Identify the blood parasite species.
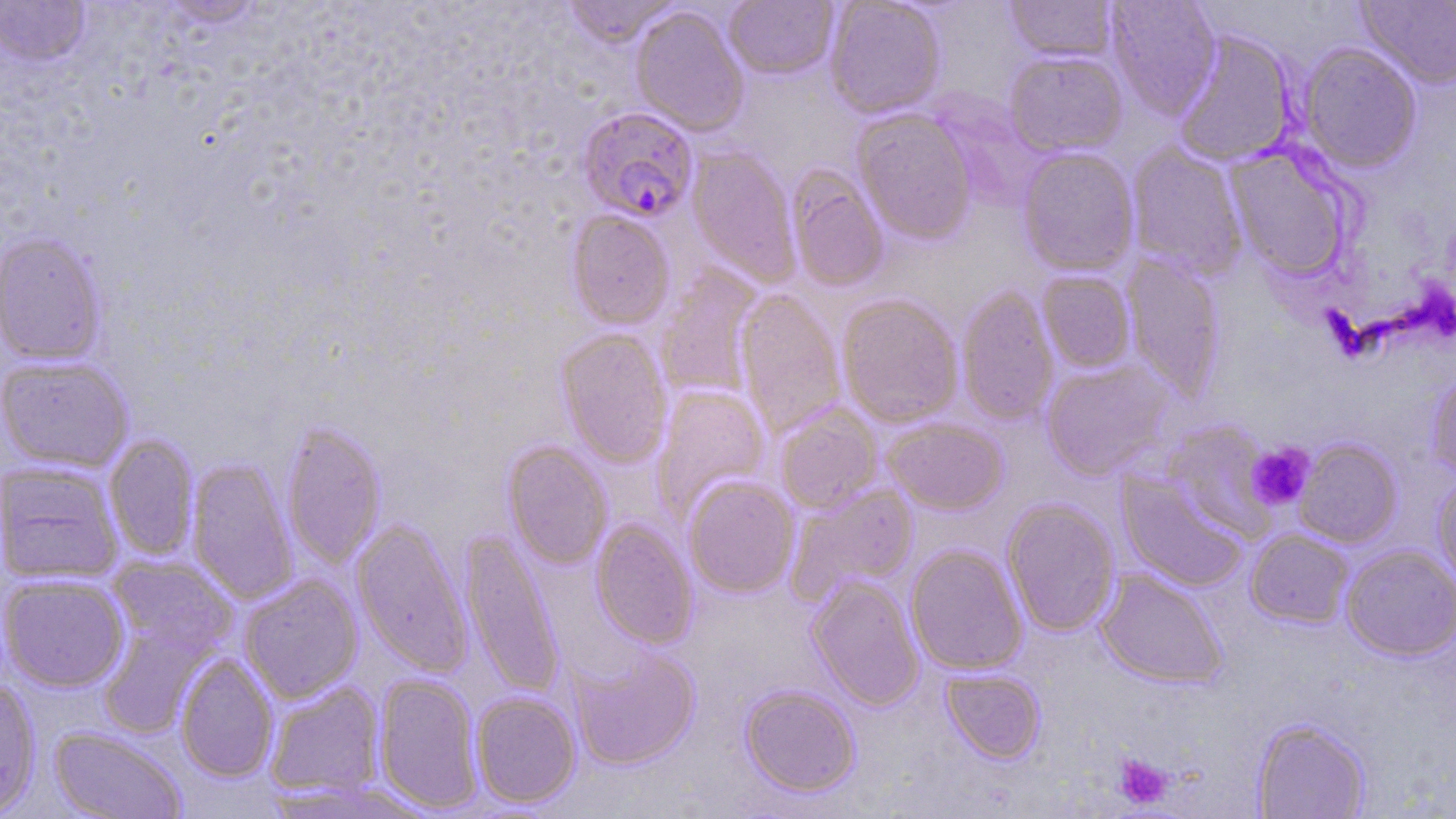
Plasmodium falciparum.

Summary:
  - Coordinate format: approximate bounding boxes as (x1,y1)-(x2,y2) corner pairs in pixels
  - Uninfected red blood cell locations: (561,0)-(681,49), (825,0)-(946,120), (1005,0)-(1117,63), (1105,0)-(1221,119), (1356,0)-(1456,89), (0,1)-(91,68), (154,1)-(268,29), (724,1)-(838,81), (630,6)-(749,137), (1172,29)-(1297,166), (1298,42)-(1422,172), (1003,51)-(1127,157), (853,108)-(978,245), (1127,144)-(1247,279), (1225,144)-(1356,282), (686,146)-(801,288), (1017,147)-(1140,277), (787,167)-(888,292), (566,211)-(675,330), (0,233)-(107,366), (1122,252)-(1225,401), (656,266)-(763,401), (1038,270)-(1136,373), (957,286)-(1058,426), (735,289)-(846,438), (837,295)-(964,428), (556,329)-(672,468), (0,356)-(134,473), (1041,359)-(1175,481), (1426,367)-(1456,481), (651,385)-(771,524), (775,404)-(883,514), (882,418)-(1008,515), (1162,420)-(1278,542), (281,421)-(386,571), (104,433)-(199,561), (1294,439)-(1402,548), (502,441)-(612,570), (186,457)-(298,606), (1,461)-(124,584), (1118,471)-(1249,591), (1432,471)-(1456,590), (683,477)-(799,597), (787,483)-(921,602), (1002,499)-(1120,637), (351,518)-(473,678), (591,519)-(698,649), (459,528)-(565,700), (1245,529)-(1355,629), (906,544)-(1028,675), (1341,544)-(1456,661), (107,555)-(237,658), (1095,569)-(1228,689), (1,573)-(130,692), (239,575)-(363,704), (806,575)-(925,711), (98,619)-(214,739), (567,644)-(701,770), (175,653)-(279,782), (941,667)-(1045,763), (373,673)-(483,813), (0,679)-(42,817), (264,681)-(385,800), (739,684)-(861,797), (470,692)-(582,809), (1252,718)-(1371,818), (49,727)-(188,819)
  - Plasmodium falciparum-infected red blood cell locations: (577,107)-(698,224)
  - Platelet locations: (1247,442)-(1315,510), (1114,753)-(1173,809)
  - Magnification: 1000x
  - Preparation: thin blood smear
  - Stain: May-Grünwald-Giemsa
  - Modality: light microscopy
  - Image size: 1456×819 pixels
  - Field of view: single